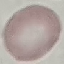
Result: no malaria parasites detected. Acquired by smartphone through the microscope eyepiece. Thin blood smear. Automatically extracted cell patch, resized to 64 × 64 pixels. Giemsa-stained preparation.